Comment on the morphology of the erythrocytes.
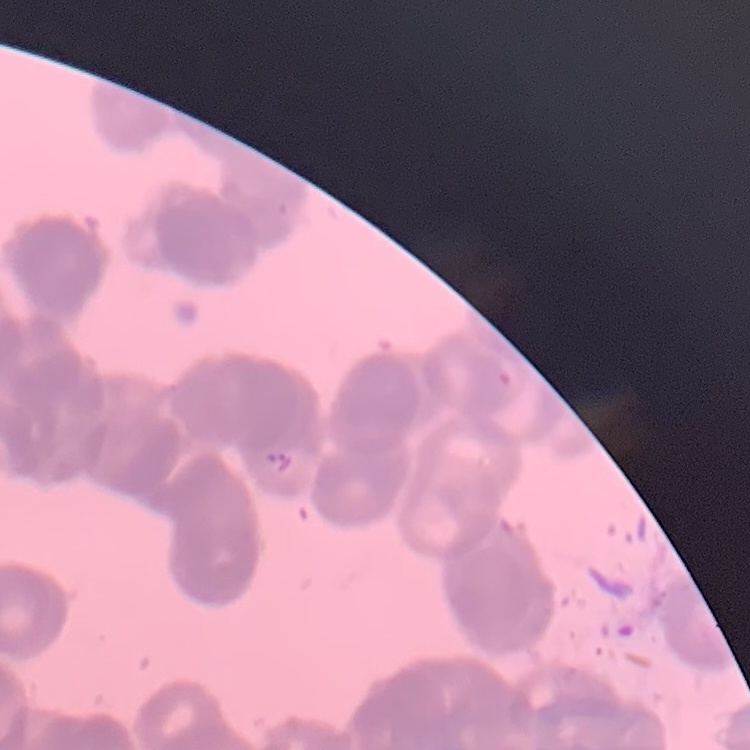

Rouleaux formation.

stain = Field's or Giemsa
preparation = thin blood film
image type = one tile cut from a larger photomicrograph